Name the parasite shown.
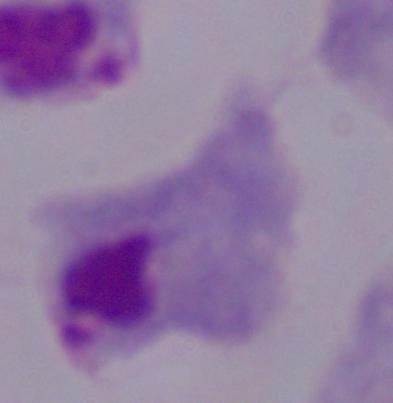
A trichomonad.

Summary:
  - Modality: micrograph
  - Magnification: 1000x